Locate every blood parasite and identify its species.
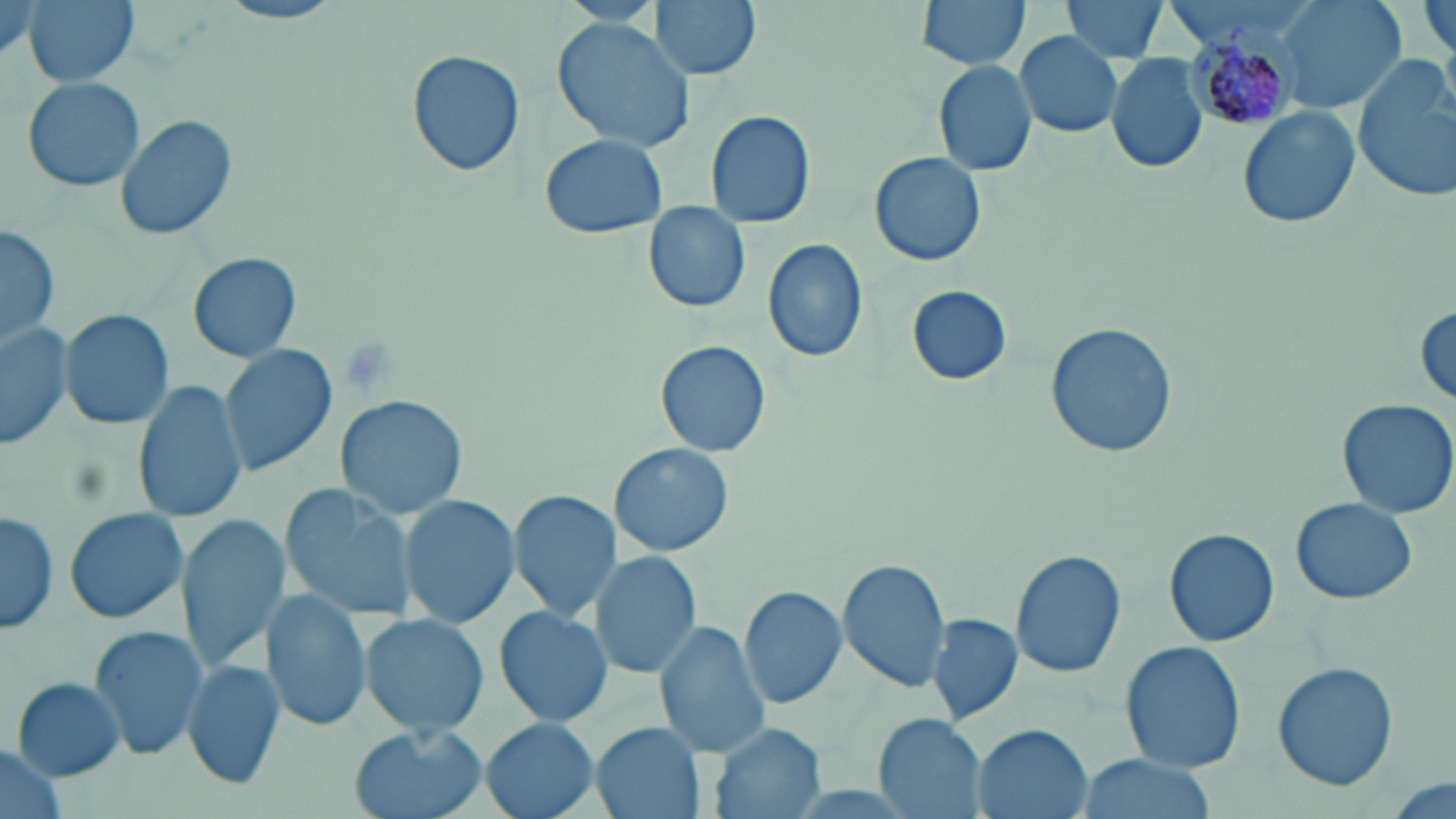
Approximate bounding boxes as (x1, y1, x2, y2) in pixels.
Plasmodium malariae-infected red blood cells: (1186, 19, 1303, 128).
No Plasmodium falciparum, Plasmodium ovale, Plasmodium vivax, Babesia divergens, or Trypanosoma brucei observed.

Uninfected red blood cell locations: (21, 0, 141, 87), (650, 0, 762, 81), (916, 0, 1033, 69), (1058, 0, 1172, 62), (1278, 0, 1407, 114), (1421, 0, 1455, 64), (215, 1, 349, 26), (552, 16, 699, 155), (1014, 32, 1125, 137), (405, 50, 525, 177), (1105, 53, 1207, 174), (1352, 55, 1456, 201), (935, 60, 1039, 176), (24, 77, 147, 192), (1238, 106, 1359, 231), (704, 108, 816, 229), (114, 113, 236, 244), (538, 134, 667, 239), (869, 151, 987, 267), (641, 201, 752, 313), (2, 224, 60, 350), (762, 239, 869, 363), (188, 252, 302, 362), (905, 285, 1014, 385), (1412, 299, 1456, 409), (60, 309, 174, 429), (0, 318, 73, 451), (1046, 322, 1177, 459), (655, 341, 773, 457), (219, 344, 337, 476), (134, 383, 248, 522), (335, 395, 470, 521), (1336, 398, 1456, 520), (611, 442, 734, 558), (278, 484, 420, 625), (509, 489, 620, 621), (399, 495, 520, 626), (1288, 496, 1418, 606), (1, 506, 59, 636), (63, 507, 189, 625), (177, 511, 290, 672), (1164, 528, 1280, 647), (1012, 549, 1128, 680), (589, 550, 699, 681), (836, 559, 951, 691), (738, 585, 848, 711), (260, 591, 372, 731), (494, 604, 614, 726), (926, 612, 1023, 726), (361, 614, 489, 738), (656, 621, 771, 759), (87, 625, 209, 762), (1120, 642, 1247, 772), (183, 659, 286, 792), (1273, 660, 1396, 792), (10, 675, 127, 780), (873, 713, 988, 818), (481, 718, 600, 819), (591, 722, 705, 819), (710, 723, 826, 819), (971, 726, 1094, 819), (350, 727, 486, 819), (0, 744, 66, 819), (1078, 755, 1212, 819), (1385, 777, 1455, 819). Slide-level diagnosis: Plasmodium malariae. May-Grünwald-Giemsa-stained preparation. 1000x magnification. One field of a larger specimen. Image is 1456×819 pixels. Thin blood smear. Light microscopy.